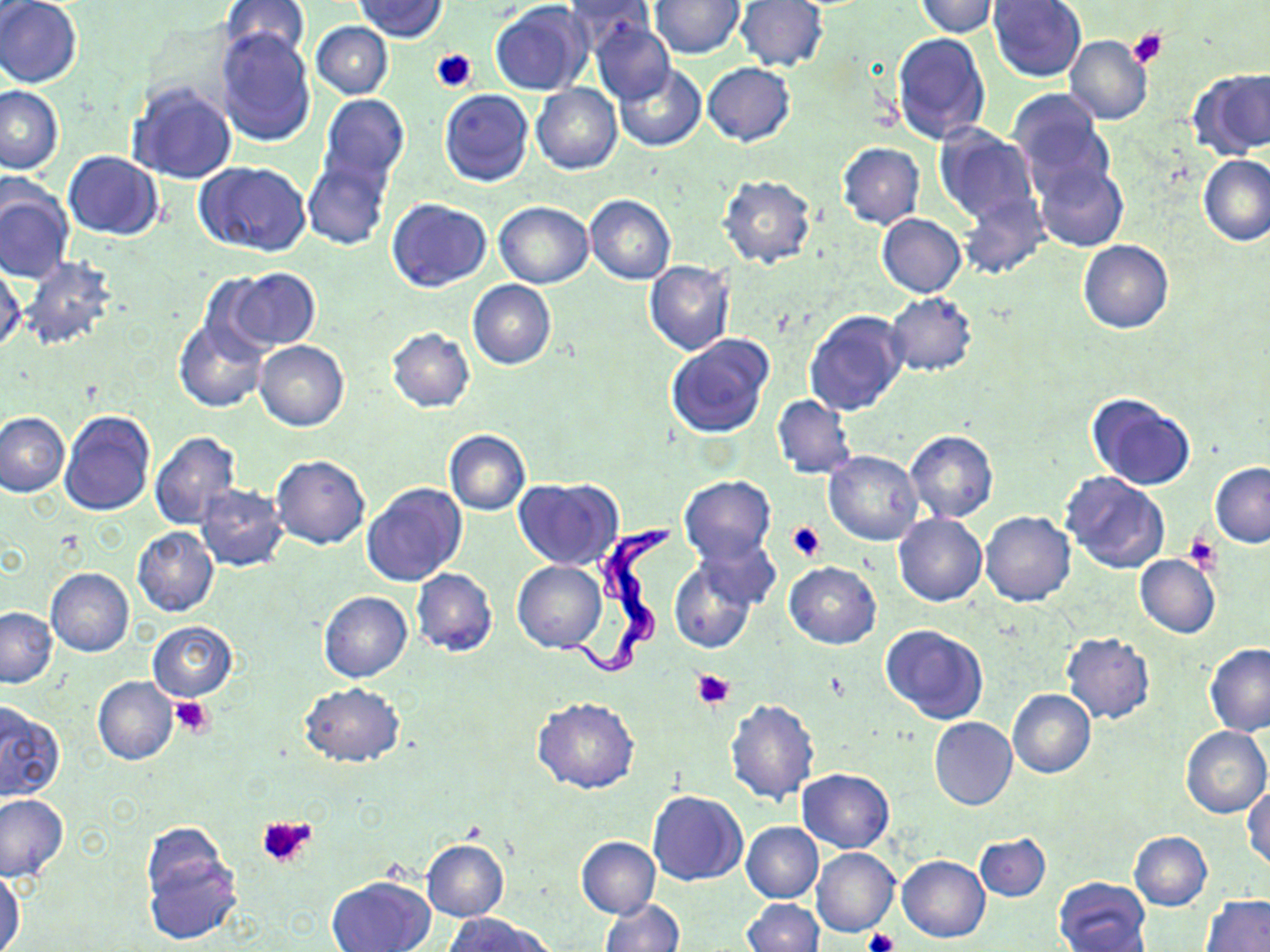

Approximate bounding boxes as named x1/y1/x2/y2 corners in pixels. Platelet locations: (x1=1127, y1=27, x2=1167, y2=67), (x1=432, y1=49, x2=477, y2=93), (x1=786, y1=520, x2=826, y2=561), (x1=1183, y1=532, x2=1222, y2=573), (x1=692, y1=669, x2=734, y2=708), (x1=171, y1=696, x2=216, y2=739), (x1=257, y1=815, x2=319, y2=871), (x1=862, y1=927, x2=899, y2=952). Uninfected red blood cell locations: (x1=1, y1=0, x2=83, y2=89), (x1=354, y1=0, x2=448, y2=40), (x1=649, y1=0, x2=743, y2=58), (x1=221, y1=1, x2=311, y2=64), (x1=565, y1=1, x2=654, y2=50), (x1=736, y1=1, x2=828, y2=72), (x1=914, y1=1, x2=996, y2=37), (x1=988, y1=1, x2=1086, y2=81), (x1=490, y1=2, x2=591, y2=96), (x1=590, y1=18, x2=675, y2=105), (x1=312, y1=21, x2=393, y2=99), (x1=215, y1=28, x2=315, y2=147), (x1=892, y1=32, x2=991, y2=146), (x1=1065, y1=34, x2=1153, y2=124), (x1=702, y1=62, x2=795, y2=146), (x1=614, y1=63, x2=706, y2=152), (x1=1188, y1=69, x2=1270, y2=158), (x1=127, y1=80, x2=238, y2=185), (x1=531, y1=83, x2=621, y2=175), (x1=0, y1=84, x2=64, y2=175), (x1=439, y1=89, x2=534, y2=187), (x1=1009, y1=92, x2=1112, y2=196), (x1=318, y1=94, x2=410, y2=191), (x1=933, y1=125, x2=1038, y2=224), (x1=837, y1=143, x2=925, y2=229), (x1=63, y1=152, x2=164, y2=238), (x1=1197, y1=155, x2=1270, y2=247), (x1=302, y1=156, x2=391, y2=251), (x1=195, y1=161, x2=310, y2=257), (x1=1034, y1=161, x2=1128, y2=252), (x1=717, y1=175, x2=818, y2=268), (x1=0, y1=182, x2=74, y2=285), (x1=959, y1=191, x2=1049, y2=278), (x1=585, y1=195, x2=675, y2=284), (x1=386, y1=198, x2=492, y2=291), (x1=495, y1=201, x2=594, y2=288), (x1=877, y1=214, x2=965, y2=298), (x1=1078, y1=239, x2=1173, y2=333), (x1=18, y1=255, x2=118, y2=352), (x1=1, y1=261, x2=25, y2=354), (x1=644, y1=261, x2=735, y2=355), (x1=222, y1=267, x2=320, y2=354), (x1=468, y1=279, x2=556, y2=369), (x1=885, y1=292, x2=976, y2=376), (x1=803, y1=308, x2=907, y2=415), (x1=174, y1=318, x2=268, y2=413), (x1=387, y1=327, x2=474, y2=412), (x1=666, y1=334, x2=775, y2=438), (x1=253, y1=340, x2=349, y2=430), (x1=1085, y1=392, x2=1197, y2=490), (x1=771, y1=394, x2=857, y2=479), (x1=59, y1=411, x2=156, y2=516), (x1=1, y1=412, x2=69, y2=497), (x1=444, y1=430, x2=531, y2=515), (x1=905, y1=430, x2=998, y2=522), (x1=149, y1=431, x2=242, y2=529), (x1=823, y1=451, x2=924, y2=545), (x1=271, y1=456, x2=370, y2=550), (x1=1210, y1=463, x2=1270, y2=547), (x1=1061, y1=472, x2=1170, y2=573), (x1=679, y1=475, x2=776, y2=564), (x1=513, y1=477, x2=624, y2=571), (x1=194, y1=483, x2=290, y2=572), (x1=361, y1=483, x2=467, y2=587), (x1=981, y1=512, x2=1076, y2=606), (x1=892, y1=513, x2=988, y2=606), (x1=132, y1=526, x2=219, y2=617), (x1=693, y1=536, x2=780, y2=611), (x1=1135, y1=555, x2=1220, y2=638), (x1=669, y1=559, x2=757, y2=653), (x1=513, y1=560, x2=606, y2=653), (x1=785, y1=562, x2=881, y2=649), (x1=411, y1=567, x2=498, y2=657), (x1=45, y1=568, x2=134, y2=657), (x1=318, y1=591, x2=413, y2=682), (x1=1, y1=607, x2=57, y2=687), (x1=148, y1=621, x2=239, y2=702), (x1=881, y1=624, x2=988, y2=724), (x1=1060, y1=632, x2=1155, y2=724), (x1=1204, y1=644, x2=1270, y2=737), (x1=93, y1=677, x2=178, y2=765), (x1=299, y1=683, x2=406, y2=767), (x1=1008, y1=689, x2=1096, y2=780), (x1=532, y1=696, x2=640, y2=794), (x1=725, y1=698, x2=819, y2=806), (x1=0, y1=699, x2=68, y2=803), (x1=929, y1=717, x2=1017, y2=811), (x1=1181, y1=725, x2=1270, y2=819), (x1=798, y1=768, x2=894, y2=853), (x1=1244, y1=783, x2=1269, y2=871), (x1=646, y1=790, x2=747, y2=885), (x1=0, y1=793, x2=68, y2=880), (x1=742, y1=821, x2=823, y2=902), (x1=1129, y1=831, x2=1212, y2=910), (x1=974, y1=832, x2=1051, y2=902), (x1=576, y1=836, x2=660, y2=918), (x1=421, y1=839, x2=509, y2=922), (x1=141, y1=844, x2=241, y2=946), (x1=812, y1=847, x2=899, y2=937), (x1=897, y1=855, x2=990, y2=943), (x1=1, y1=869, x2=26, y2=952), (x1=326, y1=875, x2=435, y2=952), (x1=1055, y1=877, x2=1150, y2=951), (x1=1202, y1=894, x2=1269, y2=952), (x1=599, y1=898, x2=684, y2=952), (x1=744, y1=900, x2=824, y2=952), (x1=446, y1=914, x2=552, y2=952). Trypanosoma brucei locations: (x1=559, y1=519, x2=674, y2=682). Slide-level diagnosis: Trypanosoma brucei. 1000x magnification. Light microscopy. Image is 1270×952 pixels. One field of a larger specimen. Thin blood film. May-Grünwald-Giemsa-stained preparation.